Describe the morphology of the red blood cells.
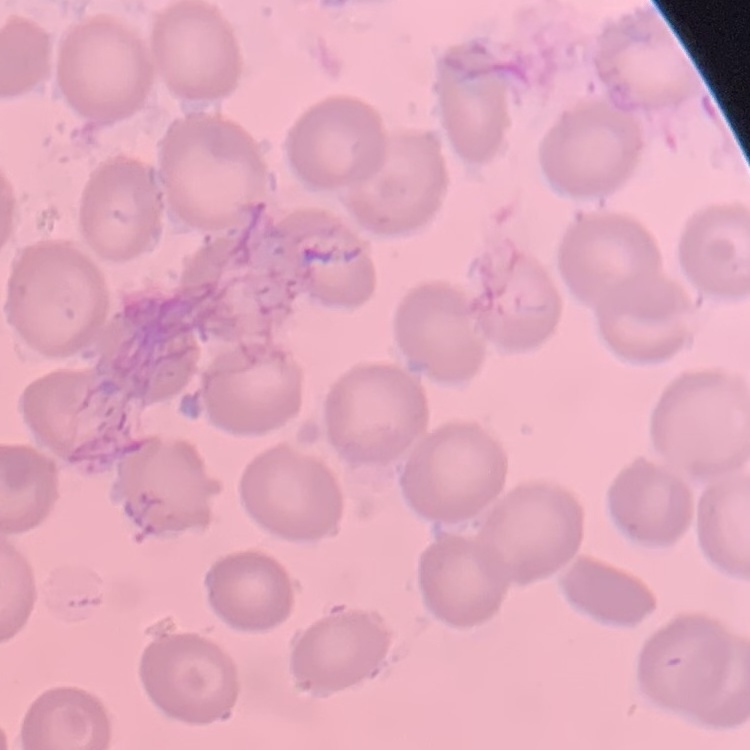

No rouleaux formation.

Summary:
  - Stain: Field's or Giemsa
  - Preparation: thin blood film
  - Image type: one tile cut from a larger photomicrograph